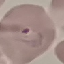

Summary:
  - Malaria status: parasitized
  - Stain: Giemsa
  - Image type: automatically extracted cell patch, resized to 64 × 64 pixels
  - Preparation: thin smear
  - Capture: smartphone through the microscope eyepiece